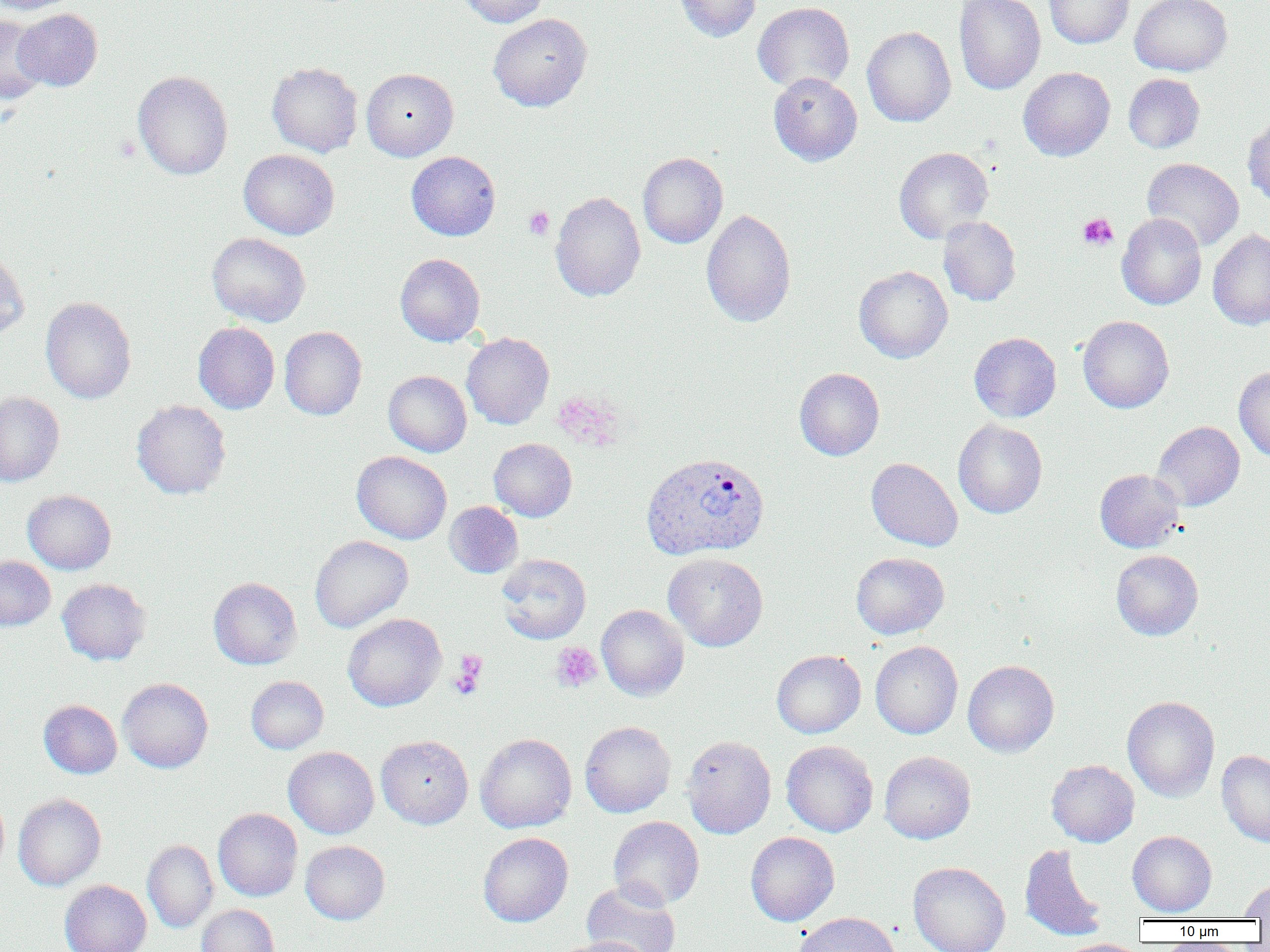
Approximate bounding boxes as (x1,y1)-(x2,y2) corner pairs in pixels. Plasmodium vivax-infected red blood cell locations: (641,452)-(769,560). Uninfected red blood cell locations: (0,0)-(79,15), (459,0)-(548,27), (673,0)-(761,42), (954,0)-(1046,95), (1044,0)-(1134,48), (1130,0)-(1232,76), (752,1)-(855,93), (14,8)-(102,91), (488,13)-(592,111), (0,14)-(47,103), (862,26)-(956,127), (266,62)-(363,157), (1018,67)-(1115,161), (361,68)-(458,161), (133,70)-(233,180), (768,72)-(862,166), (1123,73)-(1204,153), (1243,113)-(1270,209), (894,147)-(993,243), (238,149)-(339,240), (406,151)-(501,240), (638,152)-(728,248), (1142,157)-(1244,251), (550,191)-(645,302), (701,209)-(796,327), (1116,213)-(1206,310), (938,216)-(1021,306), (1208,229)-(1270,330), (207,233)-(311,327), (0,250)-(30,340), (395,253)-(485,346), (854,265)-(953,363), (40,296)-(136,404), (1078,315)-(1174,413), (193,322)-(280,414), (279,326)-(367,420), (461,332)-(554,430), (969,332)-(1061,422), (1234,366)-(1270,462), (794,368)-(884,460), (384,371)-(471,457), (0,391)-(64,486), (131,399)-(231,499), (953,420)-(1047,518), (1152,421)-(1245,511), (489,438)-(577,521), (351,451)-(452,544), (866,458)-(963,551), (1094,469)-(1184,553), (22,490)-(116,574), (444,501)-(523,578), (310,535)-(413,632), (1111,550)-(1203,640), (663,552)-(768,651), (851,552)-(949,639), (496,553)-(591,644), (0,555)-(56,630), (208,577)-(302,669), (57,579)-(152,665), (596,605)-(689,701), (343,613)-(446,711), (870,641)-(962,739), (772,650)-(866,738), (963,659)-(1059,758), (246,676)-(328,753), (118,678)-(213,773), (1122,696)-(1220,802), (39,699)-(122,778), (580,721)-(676,817), (475,733)-(577,833), (376,735)-(473,829), (682,735)-(776,838), (781,740)-(878,838), (283,746)-(379,838), (1217,750)-(1270,846), (879,751)-(976,843), (1046,759)-(1139,847), (0,788)-(9,878), (13,793)-(106,891), (213,808)-(302,901), (608,816)-(704,909), (1128,831)-(1217,917), (478,832)-(573,927), (745,832)-(840,926), (142,839)-(218,932), (300,840)-(390,924), (1019,843)-(1109,942), (908,862)-(1010,952), (60,880)-(151,952), (581,880)-(680,952), (1240,880)-(1270,919), (197,904)-(280,952), (793,912)-(900,952), (554,937)-(653,952), (1056,938)-(1147,952). Platelet locations: (524,206)-(554,239), (1078,213)-(1118,251), (551,642)-(601,692), (449,652)-(488,699). Slide-level diagnosis: Plasmodium vivax. Thin blood film. Image is 1270×952 pixels. One field of a larger specimen. Optical microscopy. 1000x magnification.